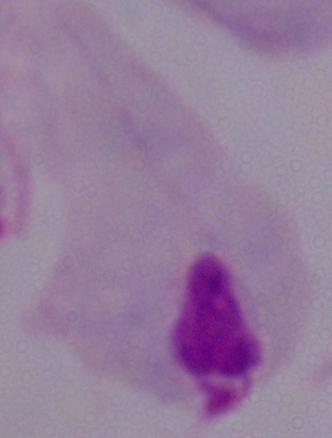
magnification: 1000x
modality: micrograph
identification: trichomonad